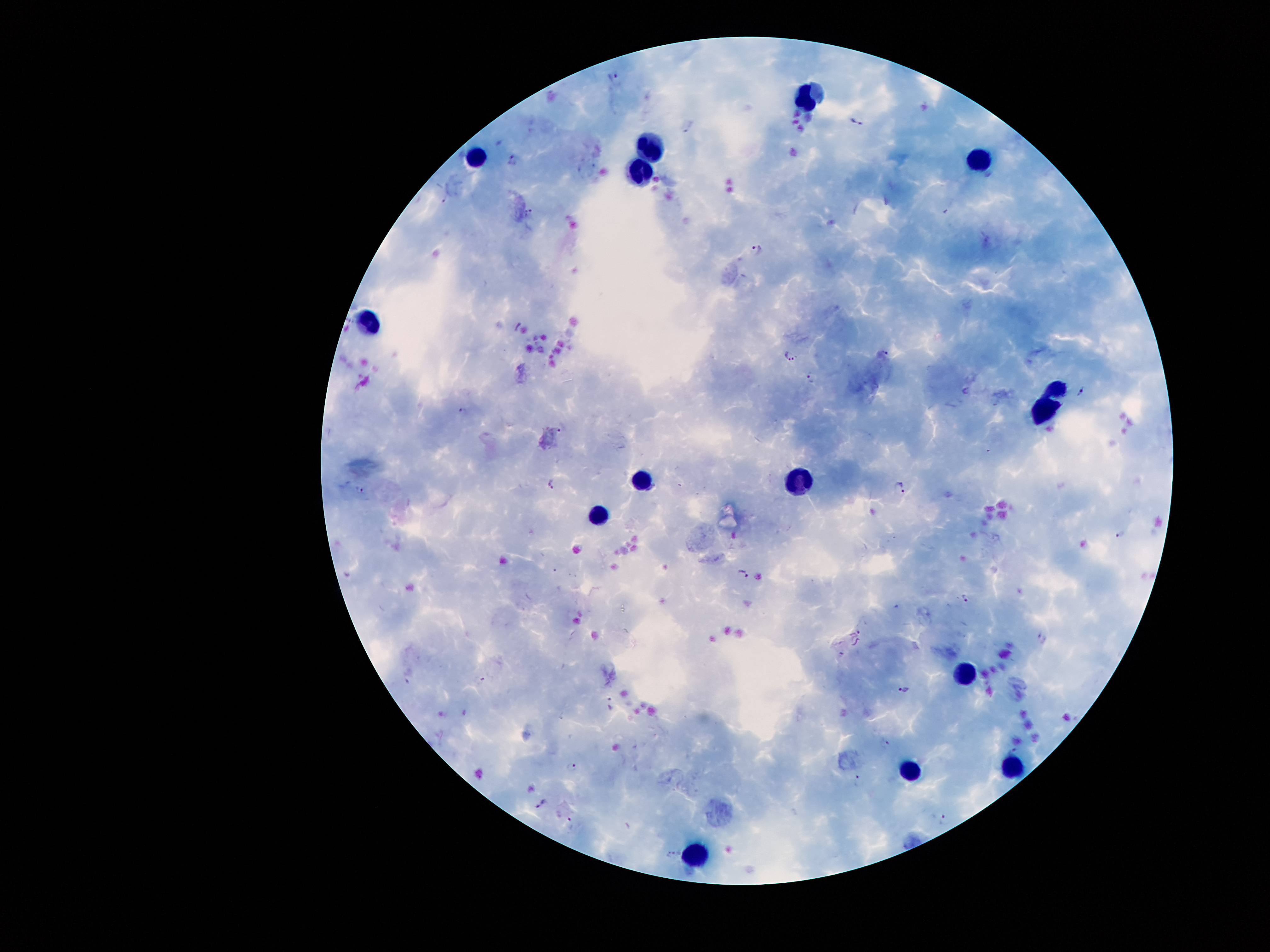

coordinate format = approximate centers as [x, y] in pixels
leukocyte locations = [804, 92], [653, 145], [473, 152], [981, 155], [638, 174], [363, 321], [1056, 386], [1042, 407], [800, 478], [640, 480], [598, 520], [964, 673], [911, 765], [1014, 767], [696, 854]
malaria parasite locations = [612, 76], [858, 120], [692, 128], [513, 159], [530, 212], [759, 248], [886, 352], [791, 354], [811, 374], [1081, 393], [465, 410], [553, 482], [900, 486], [1122, 533], [743, 572], [967, 598], [1042, 637], [904, 688], [611, 706], [887, 743], [1012, 750], [572, 768], [858, 778], [543, 806], [944, 818], [673, 855]
stain = Giemsa
magnification = 100x
capture = smartphone through the microscope eyepiece
preparation = thick blood smear
field of view = one from this slide
patient malaria status = infected with Plasmodium falciparum
image size = 1270×952 pixels